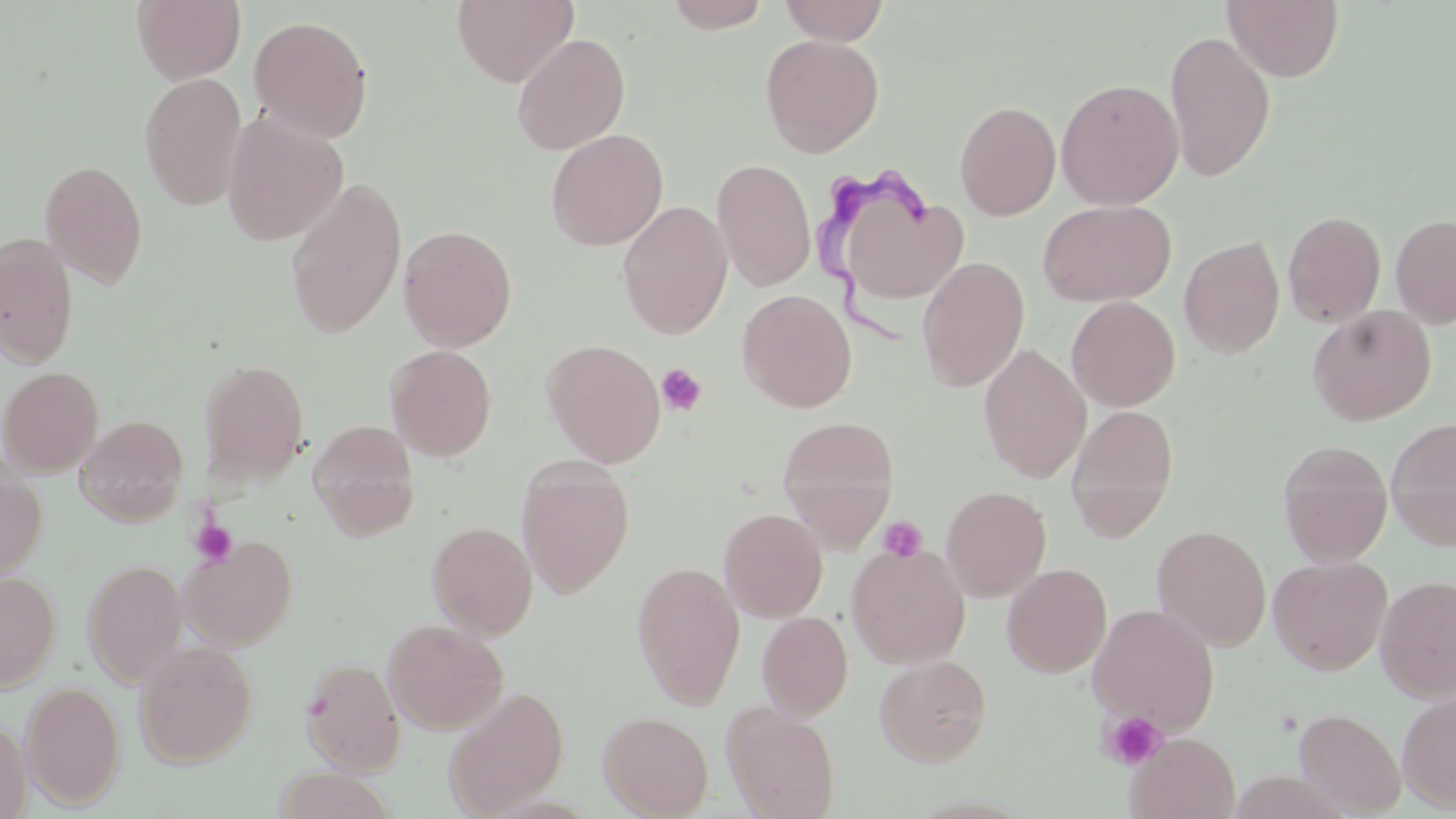

Summary:
  - Coordinate format: approximate bounding boxes as [x1, y1, x2, y2] in pixels
  - Platelet locations: [656, 364, 707, 416], [878, 516, 927, 560], [190, 520, 238, 567], [1099, 710, 1168, 771]
  - Uninfected red blood cell locations: [131, 0, 246, 84], [452, 0, 579, 87], [663, 0, 772, 32], [777, 0, 890, 45], [1222, 0, 1344, 81], [248, 15, 374, 143], [1164, 30, 1276, 183], [511, 33, 630, 154], [760, 33, 884, 157], [138, 72, 248, 211], [1056, 78, 1184, 210], [954, 100, 1060, 220], [222, 112, 348, 246], [545, 129, 668, 251], [711, 158, 816, 291], [39, 159, 149, 288], [284, 178, 406, 339], [1038, 199, 1177, 306], [617, 200, 733, 339], [845, 200, 971, 298], [1282, 210, 1386, 327], [1391, 214, 1456, 328], [398, 225, 517, 351], [0, 231, 79, 368], [1179, 235, 1285, 357], [917, 257, 1030, 391], [737, 289, 857, 412], [1066, 296, 1181, 411], [1307, 304, 1436, 425], [541, 339, 666, 467], [978, 344, 1091, 483], [385, 345, 497, 462], [198, 358, 310, 488], [0, 365, 103, 477], [1066, 404, 1179, 541], [75, 415, 188, 526], [778, 416, 900, 545], [1386, 416, 1456, 551], [308, 419, 420, 539], [1277, 439, 1393, 566], [516, 456, 635, 599], [0, 459, 47, 584], [940, 485, 1052, 601], [718, 508, 828, 622], [426, 521, 538, 639], [1152, 525, 1271, 651], [179, 536, 298, 650], [846, 544, 971, 668], [1268, 555, 1393, 675], [82, 559, 187, 687], [631, 561, 745, 708], [1002, 563, 1112, 678], [0, 571, 61, 691], [1375, 575, 1456, 703], [1087, 603, 1220, 735], [757, 611, 853, 721], [383, 618, 507, 734], [133, 640, 258, 767], [874, 653, 992, 766], [300, 657, 406, 774], [21, 681, 125, 810], [444, 685, 569, 816], [1397, 691, 1456, 812], [721, 702, 841, 819], [1293, 708, 1406, 817], [598, 710, 713, 818], [0, 714, 32, 818], [1126, 732, 1240, 818], [272, 768, 398, 818]
  - Trypanosoma brucei locations: [811, 163, 933, 357]
  - Slide-level diagnosis: Trypanosoma brucei
  - Modality: light microscopy
  - Stain: May-Grünwald-Giemsa
  - Magnification: 1000x
  - Preparation: thin blood film
  - Image size: 1456×819 pixels
  - Field of view: single